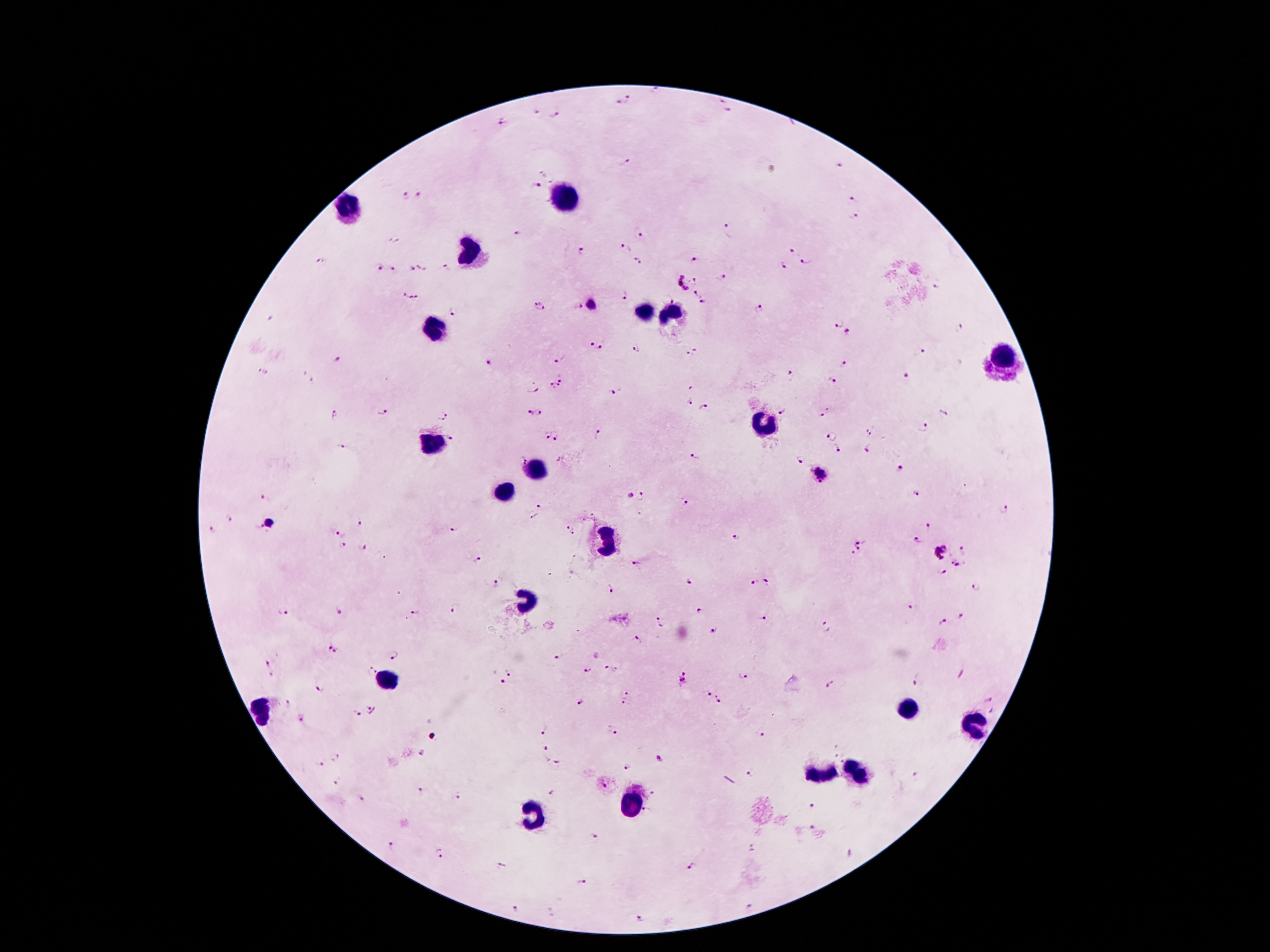
Approximate centers as {x, y} in pixels.
Summary:
  - Malaria parasite locations: {657, 94}, {630, 99}, {720, 102}, {616, 106}, {536, 112}, {728, 113}, {555, 115}, {503, 120}, {625, 162}, {839, 164}, {545, 171}, {538, 187}, {420, 194}, {405, 196}, {854, 200}, {855, 218}, {640, 231}, {729, 231}, {519, 235}, {394, 239}, {625, 247}, {792, 250}, {583, 253}, {697, 259}, {322, 260}, {636, 261}, {808, 261}, {785, 265}, {380, 266}, {412, 267}, {423, 267}, {393, 268}, {447, 269}, {698, 278}, {725, 280}, {683, 283}, {937, 287}, {698, 290}, {403, 293}, {625, 296}, {666, 296}, {416, 298}, {703, 302}, {590, 305}, {578, 306}, {539, 308}, {761, 309}, {454, 313}, {270, 320}, {837, 324}, {959, 328}, {848, 333}, {590, 344}, {601, 349}, {636, 349}, {692, 352}, {918, 352}, {561, 359}, {336, 360}, {489, 364}, {844, 365}, {261, 373}, {302, 373}, {562, 377}, {790, 377}, {906, 379}, {832, 380}, {313, 381}, {532, 388}, {555, 388}, {614, 392}, {688, 402}, {382, 410}, {704, 411}, {447, 412}, {543, 412}, {529, 413}, {822, 413}, {782, 414}, {334, 415}, {439, 419}, {922, 429}, {873, 431}, {598, 434}, {833, 434}, {545, 437}, {450, 438}, {559, 438}, {343, 446}, {837, 450}, {867, 450}, {692, 457}, {522, 460}, {800, 461}, {900, 468}, {819, 472}, {916, 494}, {643, 495}, {629, 496}, {265, 498}, {686, 503}, {541, 506}, {1004, 509}, {534, 516}, {228, 517}, {268, 523}, {361, 524}, {258, 526}, {930, 527}, {211, 528}, {566, 528}, {455, 531}, {573, 534}, {340, 535}, {737, 537}, {917, 541}, {342, 547}, {856, 548}, {363, 549}, {964, 551}, {939, 553}, {479, 561}, {950, 562}, {636, 563}, {960, 566}, {944, 573}, {689, 583}, {754, 583}, {769, 583}, {497, 584}, {612, 589}, {976, 590}, {911, 607}, {454, 609}, {340, 610}, {700, 611}, {282, 612}, {414, 612}, {762, 617}, {960, 617}, {943, 622}, {660, 623}, {828, 625}, {713, 630}, {638, 639}, {328, 642}, {338, 653}, {394, 655}, {561, 657}, {267, 663}, {612, 668}, {511, 670}, {588, 671}, {370, 672}, {271, 675}, {744, 676}, {683, 680}, {918, 680}, {498, 682}, {833, 684}, {320, 689}, {707, 693}, {628, 694}, {287, 702}, {581, 702}, {720, 702}, {621, 705}, {372, 710}, {355, 714}, {301, 718}, {543, 729}, {613, 729}, {762, 735}, {544, 749}, {424, 753}, {839, 753}, {334, 757}, {660, 757}, {841, 761}, {319, 763}, {556, 765}, {628, 766}, {751, 773}, {915, 776}, {338, 780}, {422, 790}, {653, 793}, {456, 795}, {361, 797}, {812, 805}, {646, 812}, {811, 827}, {592, 837}, {392, 847}, {850, 852}, {438, 853}, {503, 866}, {691, 866}, {582, 882}, {748, 907}, {516, 909}, {639, 918}
  - Leukocyte locations: {565, 200}, {348, 210}, {471, 253}, {643, 315}, {674, 316}, {434, 328}, {1001, 356}, {764, 424}, {434, 445}, {535, 469}, {506, 493}, {606, 542}, {524, 600}, {386, 680}, {904, 708}, {261, 711}, {973, 724}, {855, 772}, {820, 773}, {631, 801}, {530, 814}
  - Patient malaria status: infected with Plasmodium falciparum
  - Capture: smartphone through the microscope eyepiece
  - Preparation: thick peripheral-blood smear
  - Field of view: single
  - Stain: Giemsa
  - Image size: 1270×952 pixels
  - Magnification: 100x